Report the malaria status of this cell.
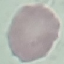

It is uninfected.

{
  "stain": "Giemsa",
  "capture": "smartphone through the microscope eyepiece",
  "preparation": "thin smear",
  "image_type": "automatically extracted cell patch, resized to 64 × 64 pixels"
}